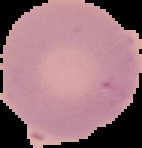 Malaria status: uninfected. From a thin blood smear. Cell region segmented out of the field of view; the surrounding area is masked to black. Image is 142×148 pixels.